State which parasite is depicted.
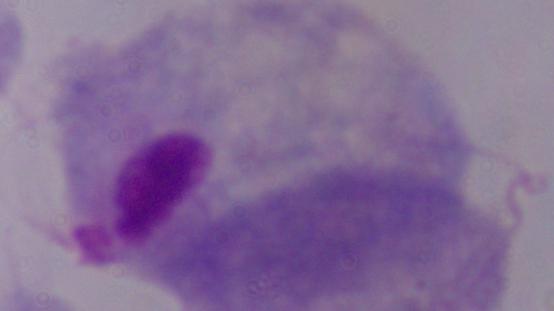
A trichomonad.

Summary:
  - Modality: micrograph
  - Magnification: 1000x